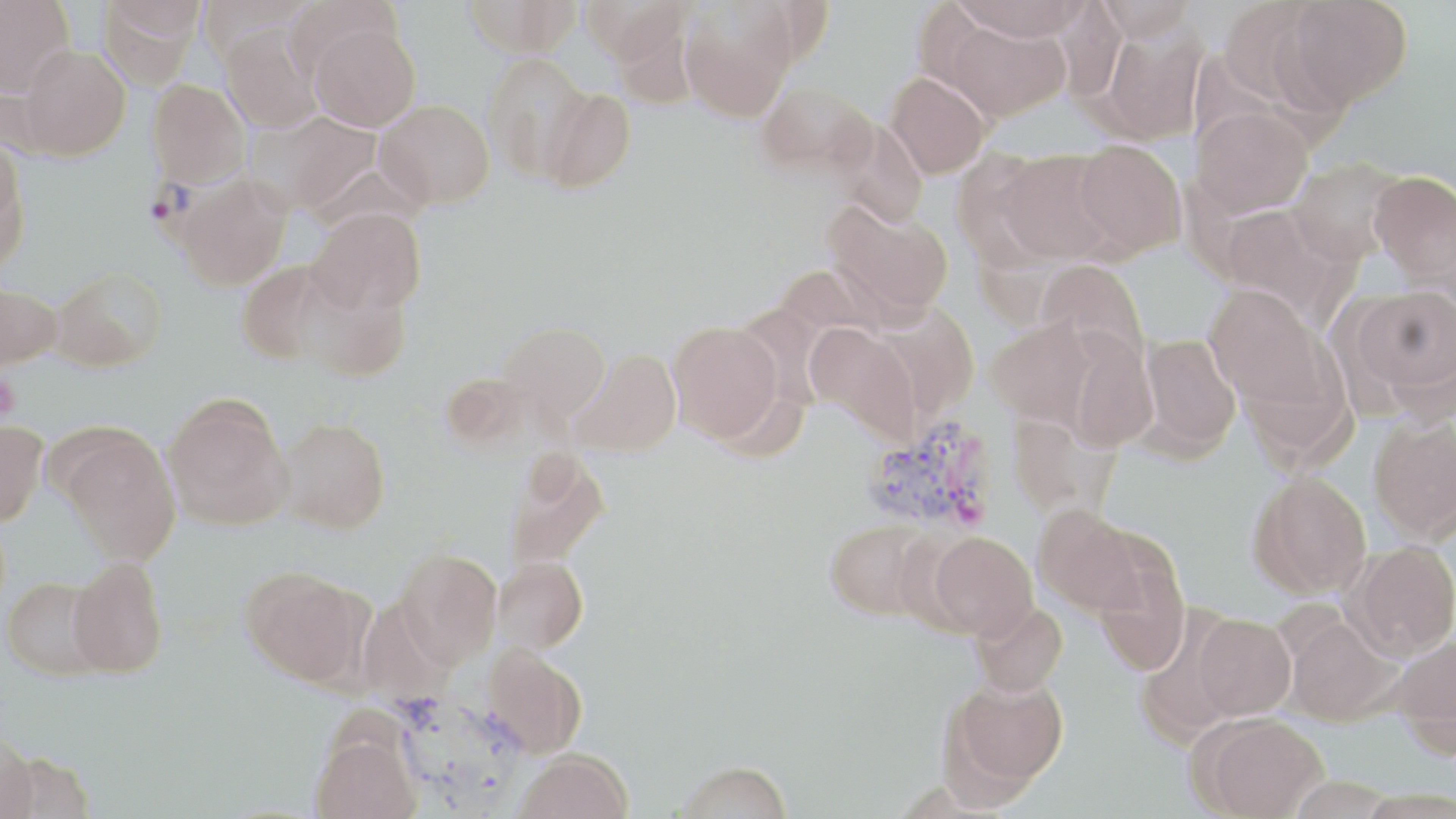
Summary:
  - Coordinate format: approximate bounding boxes as (x1, y1, x2, y2) in pixels
  - Plasmodium vivax-infected red blood cell locations: (147, 155, 253, 261), (862, 415, 1004, 535)
  - Uninfected red blood cell locations: (0, 0, 76, 95), (97, 0, 200, 90), (284, 0, 401, 83), (462, 0, 582, 56), (580, 0, 689, 63), (955, 0, 1086, 42), (1095, 0, 1196, 42), (1282, 0, 1413, 110), (679, 3, 796, 121), (946, 18, 1070, 121), (1098, 20, 1208, 144), (309, 23, 420, 131), (220, 26, 324, 133), (20, 45, 130, 159), (483, 53, 591, 180), (885, 72, 990, 178), (147, 78, 250, 188), (756, 81, 874, 175), (540, 87, 635, 192), (375, 99, 494, 209), (1191, 107, 1313, 217), (254, 111, 380, 212), (829, 117, 929, 229), (1073, 140, 1186, 257), (0, 141, 28, 271), (996, 149, 1120, 265), (950, 151, 1063, 271), (1288, 158, 1405, 264), (1369, 171, 1456, 282), (175, 176, 290, 289), (825, 200, 953, 318), (1217, 203, 1346, 320), (308, 207, 426, 316), (1037, 259, 1149, 366), (236, 260, 333, 364), (773, 265, 879, 346), (50, 267, 168, 371), (297, 273, 411, 382), (0, 282, 60, 370), (1204, 284, 1330, 412), (1351, 284, 1456, 406), (876, 301, 980, 419), (985, 319, 1096, 427), (497, 321, 610, 424), (668, 321, 785, 442), (806, 323, 921, 444), (1065, 331, 1159, 452), (1138, 333, 1241, 456), (568, 349, 681, 457), (163, 398, 291, 528), (1007, 412, 1119, 519), (1368, 415, 1456, 544), (277, 417, 390, 534), (0, 421, 48, 528), (61, 433, 180, 566), (505, 452, 612, 573), (1248, 471, 1372, 599), (1033, 505, 1146, 617), (824, 518, 937, 620), (927, 531, 1037, 640), (1345, 540, 1456, 660), (395, 550, 503, 668), (494, 556, 588, 654), (67, 557, 169, 678), (1092, 557, 1190, 675), (242, 569, 368, 688), (2, 577, 108, 682), (969, 600, 1068, 696), (1193, 614, 1296, 720), (1284, 615, 1402, 725), (1390, 635, 1456, 754), (480, 646, 587, 759), (942, 675, 1069, 797), (1197, 714, 1328, 819), (311, 732, 421, 819), (0, 736, 38, 819), (516, 750, 633, 819), (676, 761, 794, 819)
  - Platelet locations: (0, 374, 19, 422)
  - Slide-level diagnosis: Plasmodium vivax
  - Modality: light microscopy
  - Field of view: one of a larger specimen
  - Magnification: 1000x
  - Preparation: thin blood film
  - Image size: 1456×819 pixels
  - Stain: May-Grünwald-Giemsa